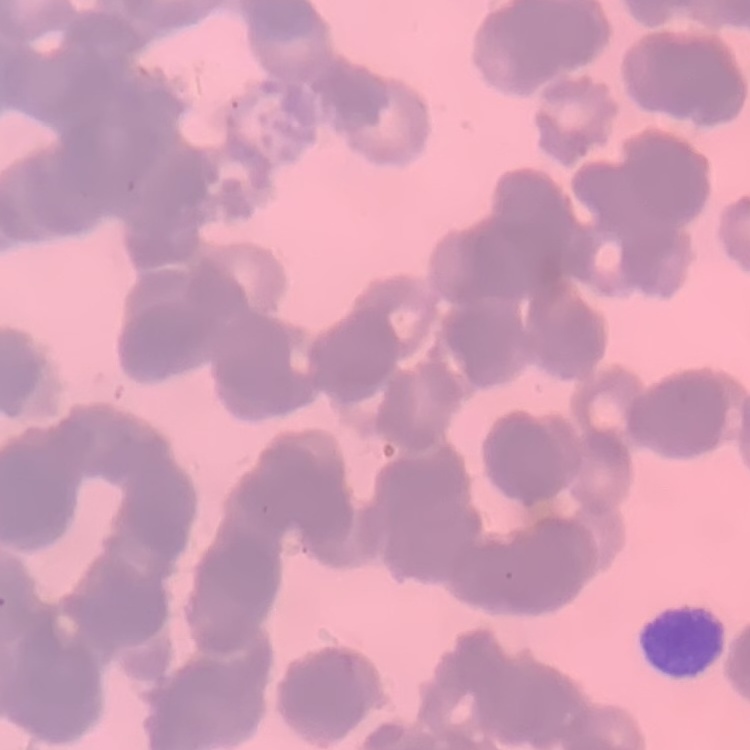

red blood cell morphology = rouleaux formation
stain = Field's or Giemsa
image type = one tile cut from a larger photomicrograph
preparation = thin blood smear